Locate and identify every blood parasite.
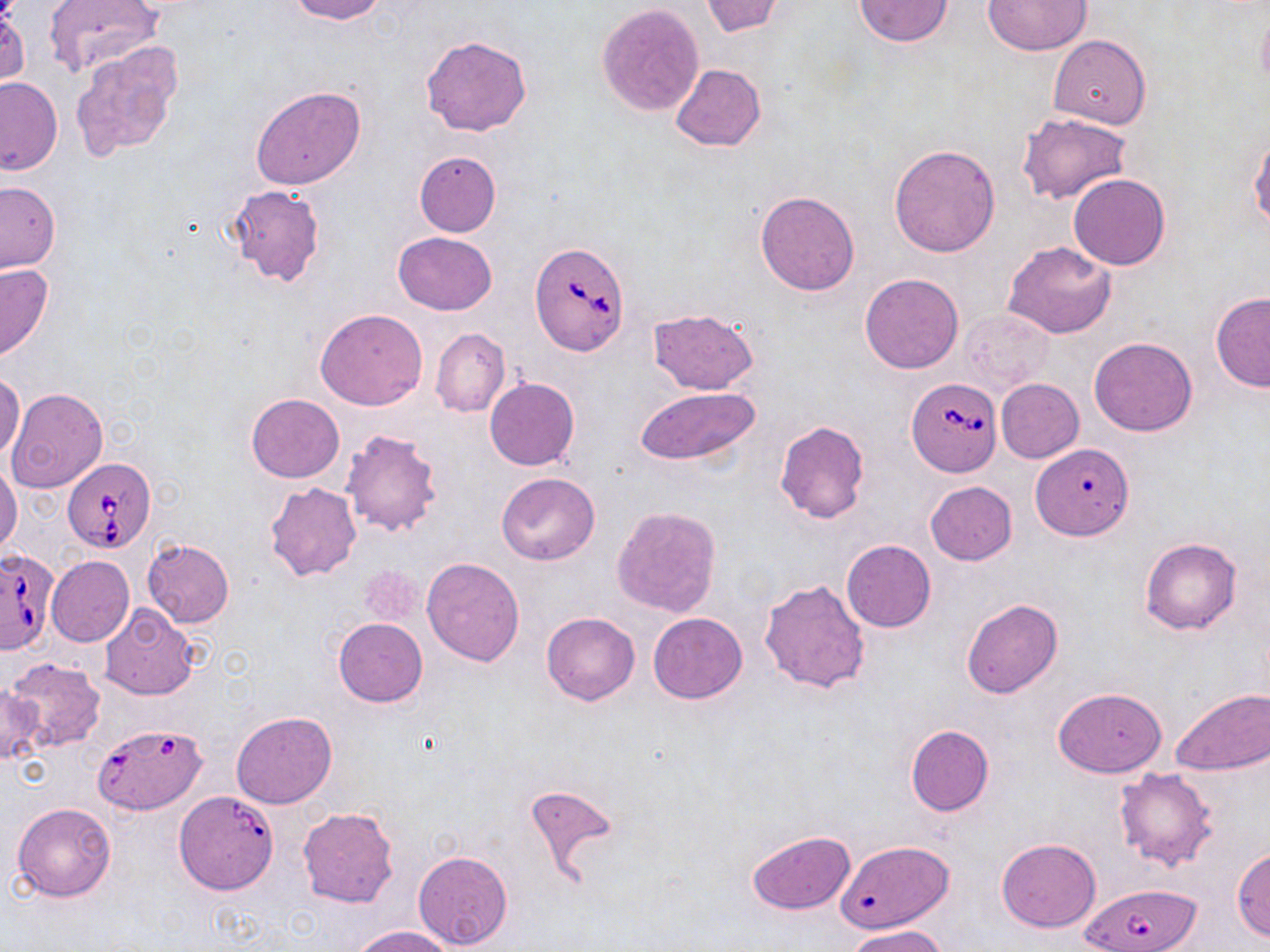

Approximate bounding boxes as named x1/y1/x2/y2 corners in pixels.
Babesia divergens-infected red blood cells: (x1=531, y1=241, x2=631, y2=355), (x1=907, y1=376, x2=1001, y2=478), (x1=64, y1=455, x2=158, y2=554), (x1=0, y1=547, x2=60, y2=658), (x1=94, y1=723, x2=207, y2=816), (x1=173, y1=790, x2=279, y2=896), (x1=1079, y1=883, x2=1202, y2=952).
No Plasmodium falciparum, Plasmodium ovale, Plasmodium malariae, Plasmodium vivax, or Trypanosoma brucei observed.

Uninfected red blood cell locations: (x1=42, y1=0, x2=163, y2=78), (x1=287, y1=0, x2=388, y2=23), (x1=700, y1=0, x2=784, y2=38), (x1=853, y1=0, x2=955, y2=49), (x1=983, y1=0, x2=1091, y2=54), (x1=597, y1=4, x2=705, y2=116), (x1=1255, y1=8, x2=1270, y2=93), (x1=1049, y1=34, x2=1151, y2=128), (x1=421, y1=35, x2=533, y2=137), (x1=71, y1=42, x2=182, y2=162), (x1=670, y1=63, x2=766, y2=152), (x1=0, y1=77, x2=62, y2=174), (x1=250, y1=85, x2=367, y2=190), (x1=1016, y1=111, x2=1132, y2=205), (x1=1248, y1=135, x2=1269, y2=231), (x1=889, y1=143, x2=1002, y2=257), (x1=415, y1=151, x2=501, y2=237), (x1=1067, y1=173, x2=1171, y2=270), (x1=0, y1=182, x2=61, y2=273), (x1=226, y1=184, x2=325, y2=287), (x1=755, y1=190, x2=861, y2=296), (x1=393, y1=232, x2=497, y2=314), (x1=1003, y1=241, x2=1116, y2=339), (x1=0, y1=263, x2=54, y2=363), (x1=860, y1=272, x2=964, y2=374), (x1=1210, y1=292, x2=1270, y2=392), (x1=647, y1=308, x2=759, y2=395), (x1=315, y1=309, x2=428, y2=411), (x1=958, y1=309, x2=1055, y2=394), (x1=430, y1=329, x2=510, y2=417), (x1=1088, y1=336, x2=1199, y2=436), (x1=1, y1=371, x2=25, y2=462), (x1=484, y1=377, x2=579, y2=471), (x1=996, y1=379, x2=1084, y2=463), (x1=635, y1=385, x2=760, y2=467), (x1=7, y1=387, x2=108, y2=494), (x1=245, y1=394, x2=344, y2=483), (x1=773, y1=421, x2=869, y2=524), (x1=340, y1=428, x2=443, y2=537), (x1=1030, y1=444, x2=1136, y2=549), (x1=0, y1=459, x2=23, y2=555), (x1=494, y1=472, x2=601, y2=565), (x1=925, y1=481, x2=1017, y2=565), (x1=264, y1=483, x2=361, y2=582), (x1=612, y1=505, x2=722, y2=619), (x1=1140, y1=537, x2=1242, y2=635), (x1=142, y1=539, x2=234, y2=627), (x1=842, y1=539, x2=936, y2=632), (x1=46, y1=556, x2=133, y2=647), (x1=421, y1=556, x2=524, y2=666), (x1=357, y1=564, x2=424, y2=628), (x1=759, y1=578, x2=871, y2=694), (x1=960, y1=598, x2=1063, y2=698), (x1=99, y1=605, x2=199, y2=700), (x1=541, y1=612, x2=640, y2=706), (x1=647, y1=613, x2=747, y2=703), (x1=333, y1=617, x2=427, y2=707), (x1=6, y1=657, x2=107, y2=753), (x1=0, y1=685, x2=45, y2=767), (x1=1052, y1=687, x2=1167, y2=778), (x1=1170, y1=688, x2=1270, y2=776), (x1=230, y1=711, x2=336, y2=808), (x1=905, y1=725, x2=994, y2=817), (x1=1112, y1=767, x2=1219, y2=872), (x1=523, y1=781, x2=622, y2=884), (x1=11, y1=803, x2=116, y2=902), (x1=299, y1=807, x2=399, y2=907), (x1=745, y1=830, x2=856, y2=914), (x1=995, y1=839, x2=1102, y2=932), (x1=838, y1=841, x2=960, y2=934), (x1=1232, y1=846, x2=1270, y2=942), (x1=413, y1=850, x2=514, y2=950), (x1=350, y1=925, x2=459, y2=952), (x1=846, y1=925, x2=949, y2=952). Slide-level diagnosis: Babesia divergens. Captured at 1000x magnification. One field of a larger specimen. Light microscopy. May-Grünwald-Giemsa-stained preparation. Image is 1270×952 pixels. Thin blood film.